Name the blood parasite species.
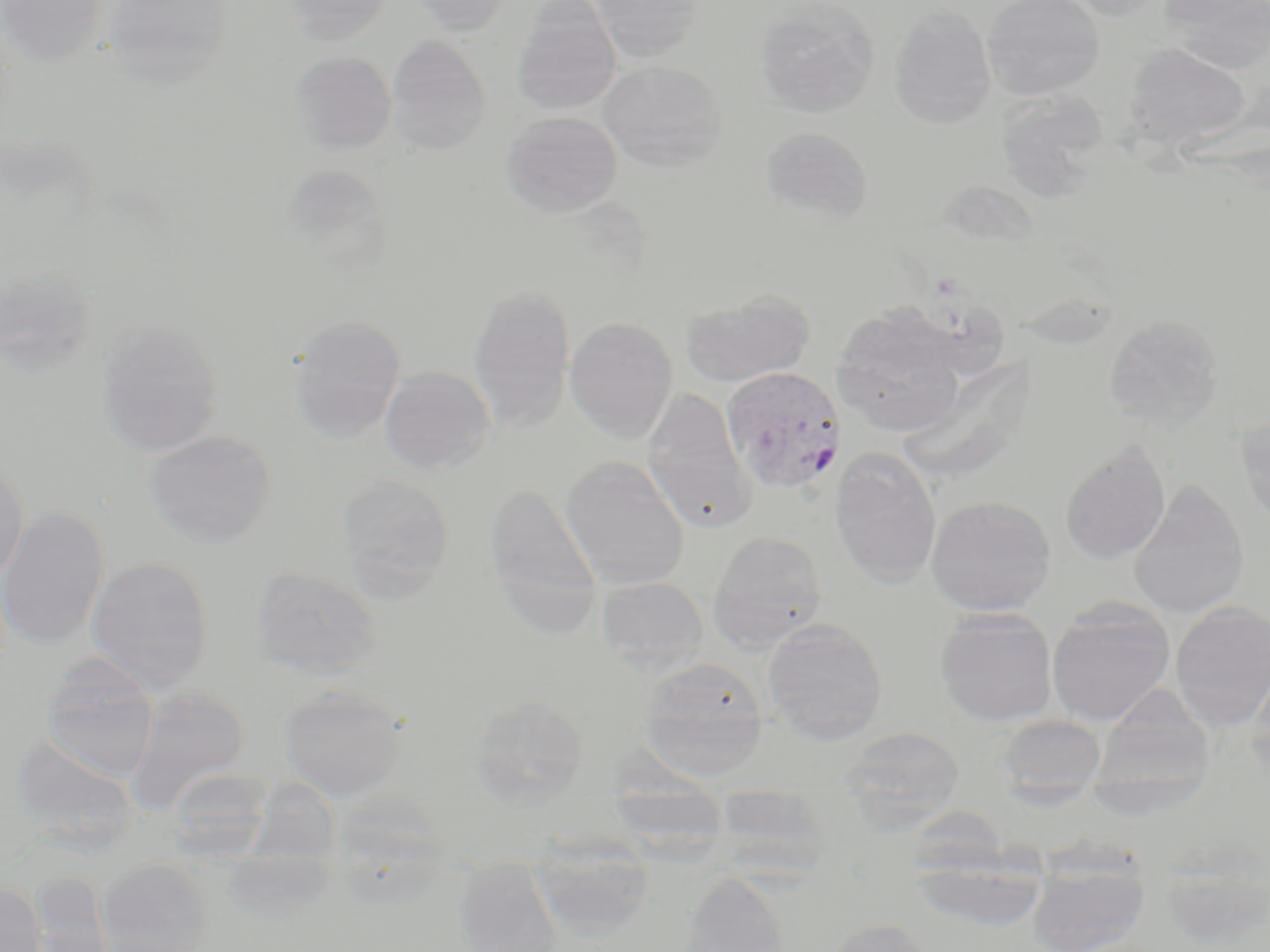

Plasmodium vivax.

magnification = 1000x
stain = May-Grünwald-Giemsa
preparation = thin blood smear
modality = optical microscopy
Plasmodium vivax-infected red blood cell locations = approximate bounding boxes as named x1/y1/x2/y2 corners in pixels: (x1=721, y1=366, x2=847, y2=493)
field of view = single
image size = 1270×952 pixels
uninfected red blood cell locations = approximate bounding boxes as named x1/y1/x2/y2 corners in pixels: (x1=0, y1=0, x2=109, y2=65), (x1=103, y1=0, x2=233, y2=89), (x1=281, y1=0, x2=395, y2=45), (x1=407, y1=0, x2=511, y2=35), (x1=587, y1=0, x2=705, y2=61), (x1=982, y1=0, x2=1104, y2=100), (x1=1061, y1=0, x2=1171, y2=20), (x1=1161, y1=0, x2=1270, y2=73), (x1=511, y1=1, x2=621, y2=115), (x1=755, y1=1, x2=879, y2=118), (x1=888, y1=6, x2=996, y2=128), (x1=386, y1=36, x2=491, y2=155), (x1=1123, y1=42, x2=1251, y2=151), (x1=290, y1=51, x2=397, y2=154), (x1=599, y1=61, x2=727, y2=171), (x1=995, y1=92, x2=1109, y2=199), (x1=501, y1=111, x2=622, y2=217), (x1=760, y1=127, x2=873, y2=224), (x1=0, y1=265, x2=98, y2=376), (x1=468, y1=284, x2=576, y2=432), (x1=680, y1=289, x2=815, y2=387), (x1=832, y1=304, x2=969, y2=438), (x1=1104, y1=314, x2=1224, y2=430), (x1=288, y1=315, x2=407, y2=442), (x1=565, y1=316, x2=678, y2=441), (x1=97, y1=319, x2=225, y2=457), (x1=898, y1=355, x2=1034, y2=484), (x1=379, y1=366, x2=496, y2=475), (x1=641, y1=388, x2=753, y2=531), (x1=1234, y1=409, x2=1270, y2=528), (x1=143, y1=429, x2=277, y2=548), (x1=1060, y1=440, x2=1170, y2=565), (x1=829, y1=448, x2=942, y2=588), (x1=560, y1=457, x2=691, y2=589), (x1=0, y1=458, x2=30, y2=586), (x1=337, y1=474, x2=455, y2=595), (x1=1128, y1=479, x2=1250, y2=618), (x1=485, y1=481, x2=603, y2=634), (x1=925, y1=495, x2=1056, y2=616), (x1=0, y1=506, x2=109, y2=651), (x1=707, y1=530, x2=828, y2=650), (x1=86, y1=556, x2=214, y2=691), (x1=251, y1=565, x2=381, y2=678), (x1=596, y1=576, x2=709, y2=670), (x1=1046, y1=600, x2=1176, y2=727), (x1=1169, y1=602, x2=1269, y2=728), (x1=934, y1=609, x2=1058, y2=727), (x1=762, y1=618, x2=887, y2=744), (x1=1248, y1=652, x2=1270, y2=776), (x1=639, y1=657, x2=768, y2=777), (x1=41, y1=658, x2=160, y2=780), (x1=279, y1=686, x2=408, y2=800), (x1=125, y1=687, x2=252, y2=814), (x1=1091, y1=692, x2=1218, y2=801), (x1=469, y1=695, x2=589, y2=806), (x1=997, y1=716, x2=1107, y2=798), (x1=839, y1=726, x2=966, y2=831), (x1=166, y1=770, x2=273, y2=861), (x1=335, y1=777, x2=452, y2=907), (x1=235, y1=778, x2=349, y2=926), (x1=529, y1=836, x2=655, y2=941), (x1=1026, y1=848, x2=1151, y2=952), (x1=911, y1=856, x2=1048, y2=934), (x1=455, y1=857, x2=563, y2=952), (x1=97, y1=858, x2=213, y2=952), (x1=678, y1=870, x2=792, y2=952), (x1=24, y1=871, x2=115, y2=951), (x1=0, y1=883, x2=47, y2=951), (x1=824, y1=917, x2=935, y2=952)